Report the malaria status of this cell.
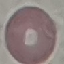

It is uninfected.

Giemsa-stained preparation. Cell patch, automatically extracted from a larger field of view and resized to 64 × 64 pixels. Thin smear of blood. Acquired by smartphone through the microscope eyepiece.